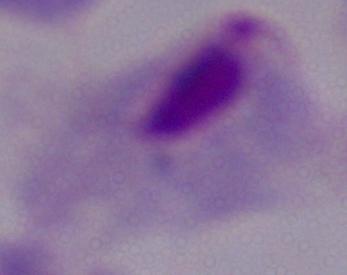

identification: trichomonad
modality: micrograph
magnification: 1000x